Classify this cell by malaria status.
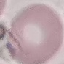
It is uninfected.

Cell patch, automatically extracted from a larger field of view and resized to 64 × 64 pixels. Acquired by smartphone through the microscope eyepiece. Giemsa stain. Thin blood smear.